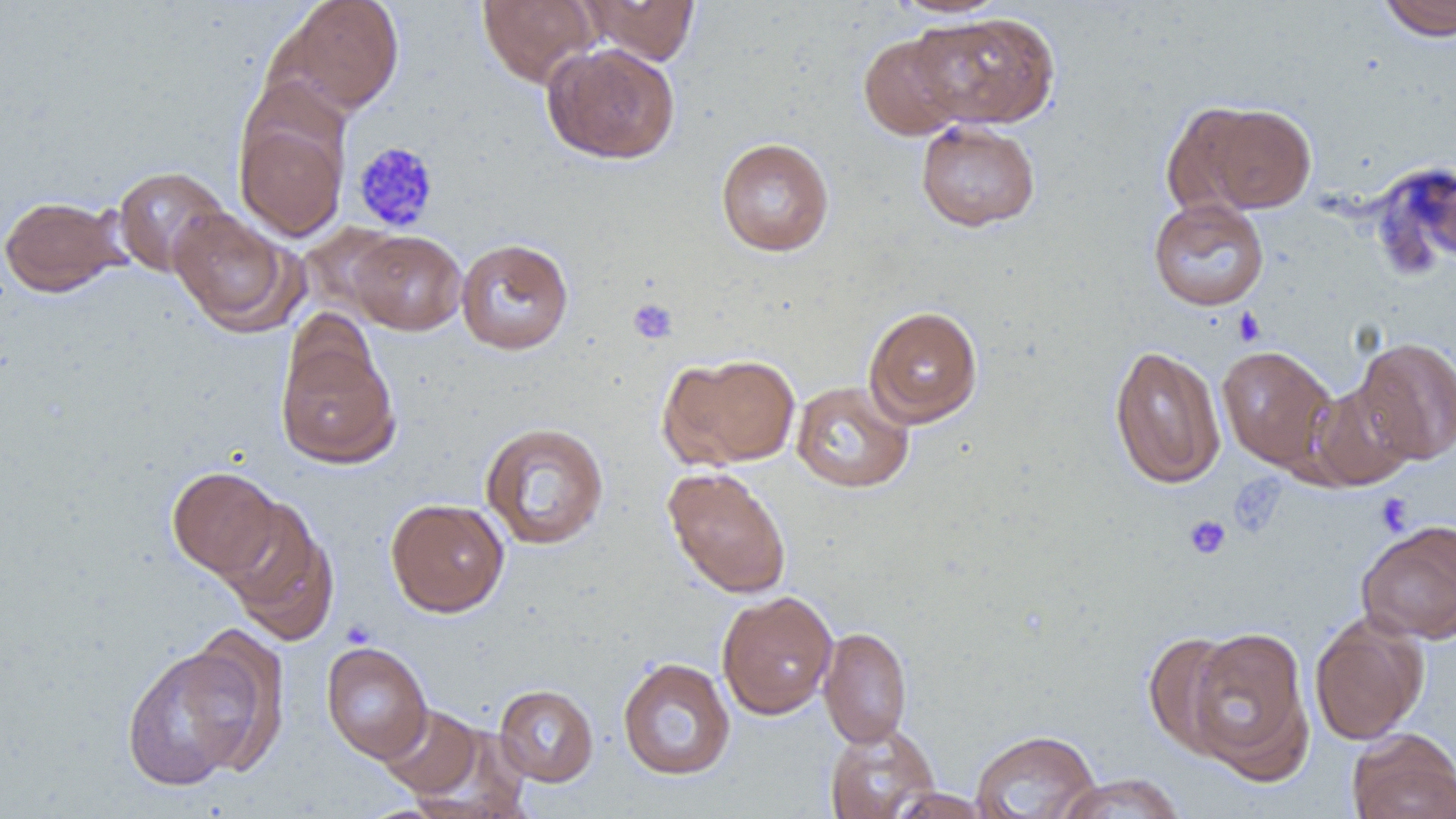

Summary:
  - Coordinate format: approximate bounding boxes as (x1,y1)-(x2,y2) corner pairs in pixels
  - Uninfected red blood cell locations: (270,0)-(406,117), (477,0)-(601,87), (580,0)-(701,64), (887,0)-(1010,17), (1376,0)-(1456,40), (909,11)-(1061,129), (858,33)-(967,140), (542,42)-(681,164), (1178,99)-(1319,215), (234,113)-(349,242), (915,120)-(1041,232), (715,136)-(835,257), (1374,161)-(1456,275), (111,165)-(231,279), (0,195)-(128,297), (1148,198)-(1269,311), (168,207)-(301,335), (297,223)-(405,319), (349,230)-(467,335), (455,237)-(574,354), (863,306)-(983,427), (276,336)-(399,470), (1353,336)-(1456,465), (1109,344)-(1226,489), (1216,344)-(1337,470), (659,352)-(802,469), (791,380)-(914,493), (1307,381)-(1418,491), (480,421)-(610,550), (167,465)-(284,579), (663,467)-(792,598), (385,497)-(510,617), (216,498)-(340,646), (1356,519)-(1456,644), (716,590)-(838,720), (1309,614)-(1429,745), (818,626)-(912,748), (1183,626)-(1313,779), (1143,631)-(1243,757), (320,641)-(433,763), (121,642)-(270,790), (617,656)-(736,781), (494,684)-(599,786), (377,704)-(485,798), (409,722)-(532,817), (824,723)-(940,819), (970,729)-(1101,818), (1347,729)-(1456,819), (1055,773)-(1187,819), (886,787)-(995,818)
  - Platelet locations: (351,140)-(440,232), (628,297)-(678,344), (1232,306)-(1266,347), (1228,473)-(1287,539), (1374,493)-(1414,535), (1184,514)-(1232,560)
  - Slide-level diagnosis: no evidence of blood parasites
  - Preparation: thin blood film
  - Magnification: 1000x
  - Modality: optical microscopy
  - Field of view: one of a larger specimen
  - Image size: 1456×819 pixels